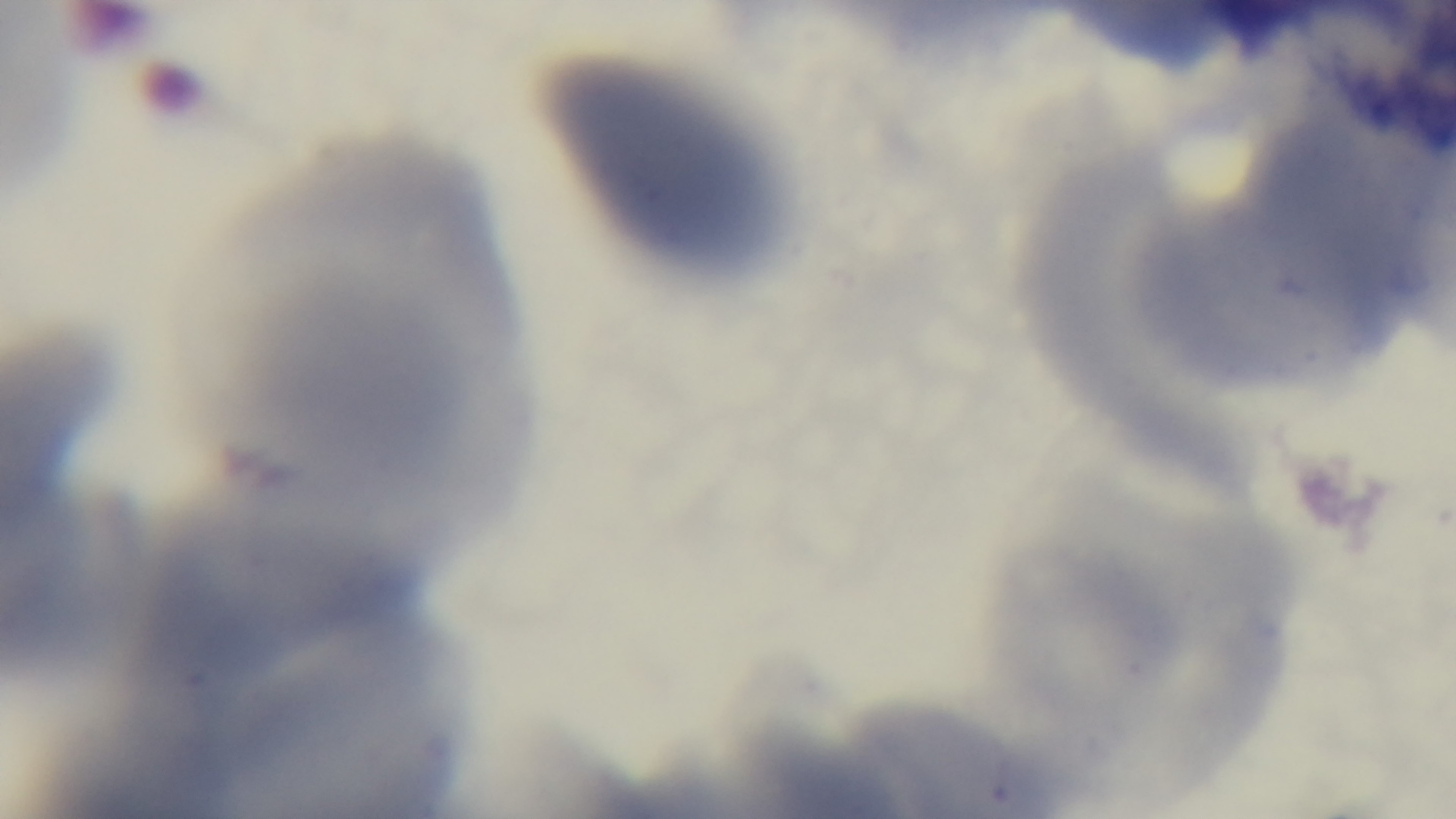

objective = 100x oil immersion
capture = mounted 4K digital camera
modality = light microscopy
stain = Giemsa
preparation = thin
field of view = single
malaria status = uninfected